Locate every Plasmodium vivax-infected red blood cell.
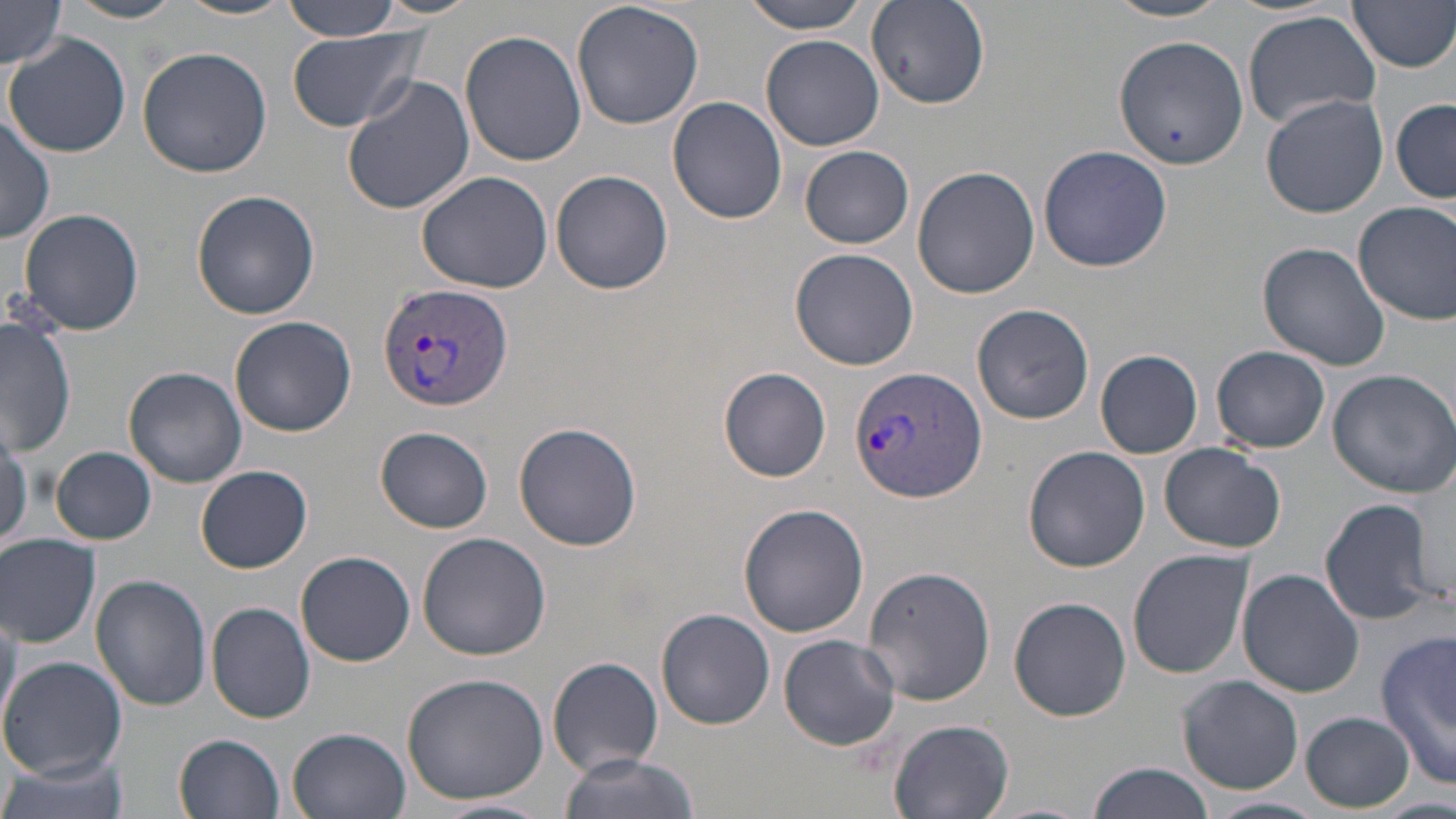

Approximate bounding boxes as [x1, y1, x2, y2] in pixels.
Plasmodium vivax-infected red blood cells: [377, 281, 513, 413], [849, 365, 987, 503].

Uninfected red blood cell locations: [67, 0, 187, 23], [176, 0, 298, 20], [367, 0, 487, 21], [572, 0, 704, 132], [742, 0, 877, 34], [1104, 0, 1236, 22], [1349, 0, 1456, 74], [279, 1, 407, 42], [866, 1, 991, 110], [1, 2, 66, 69], [1243, 9, 1382, 128], [284, 29, 426, 133], [460, 29, 587, 167], [4, 32, 131, 158], [760, 34, 886, 151], [1113, 35, 1246, 171], [137, 46, 273, 179], [342, 74, 477, 215], [1260, 93, 1388, 217], [668, 96, 788, 223], [1391, 98, 1455, 203], [0, 113, 55, 243], [801, 145, 913, 248], [1038, 145, 1172, 271], [911, 166, 1039, 300], [415, 169, 554, 294], [551, 170, 673, 296], [191, 190, 321, 320], [1354, 200, 1456, 324], [16, 207, 145, 336], [1256, 242, 1390, 371], [789, 247, 919, 371], [971, 302, 1094, 427], [2, 315, 75, 455], [229, 315, 357, 437], [1212, 345, 1328, 455], [1095, 350, 1204, 458], [123, 366, 248, 487], [719, 366, 834, 483], [1326, 369, 1456, 498], [513, 421, 642, 552], [0, 422, 30, 551], [375, 426, 494, 533], [1159, 442, 1285, 554], [52, 445, 157, 543], [1022, 445, 1153, 575], [195, 464, 313, 573], [1317, 496, 1443, 627], [738, 503, 870, 637], [416, 532, 551, 661], [0, 535, 101, 647], [296, 550, 415, 666], [1128, 550, 1255, 681], [862, 565, 995, 707], [1237, 570, 1363, 697], [92, 574, 212, 710], [1008, 597, 1130, 722], [206, 602, 315, 723], [0, 606, 21, 735], [657, 610, 775, 729], [1376, 629, 1456, 786], [778, 635, 902, 752], [0, 656, 125, 781], [548, 657, 664, 776], [400, 672, 551, 805], [1176, 675, 1303, 793], [1302, 710, 1413, 811], [888, 719, 1014, 819], [288, 727, 411, 819], [174, 733, 284, 818], [560, 753, 698, 819], [0, 754, 130, 819], [1087, 762, 1214, 819], [1205, 796, 1328, 819], [433, 800, 553, 818]. Slide-level diagnosis: Plasmodium vivax. Thin blood smear. Light microscopy. 1000x magnification. Image is 1456×819 pixels. May-Grünwald-Giemsa stain. One field of a larger specimen.